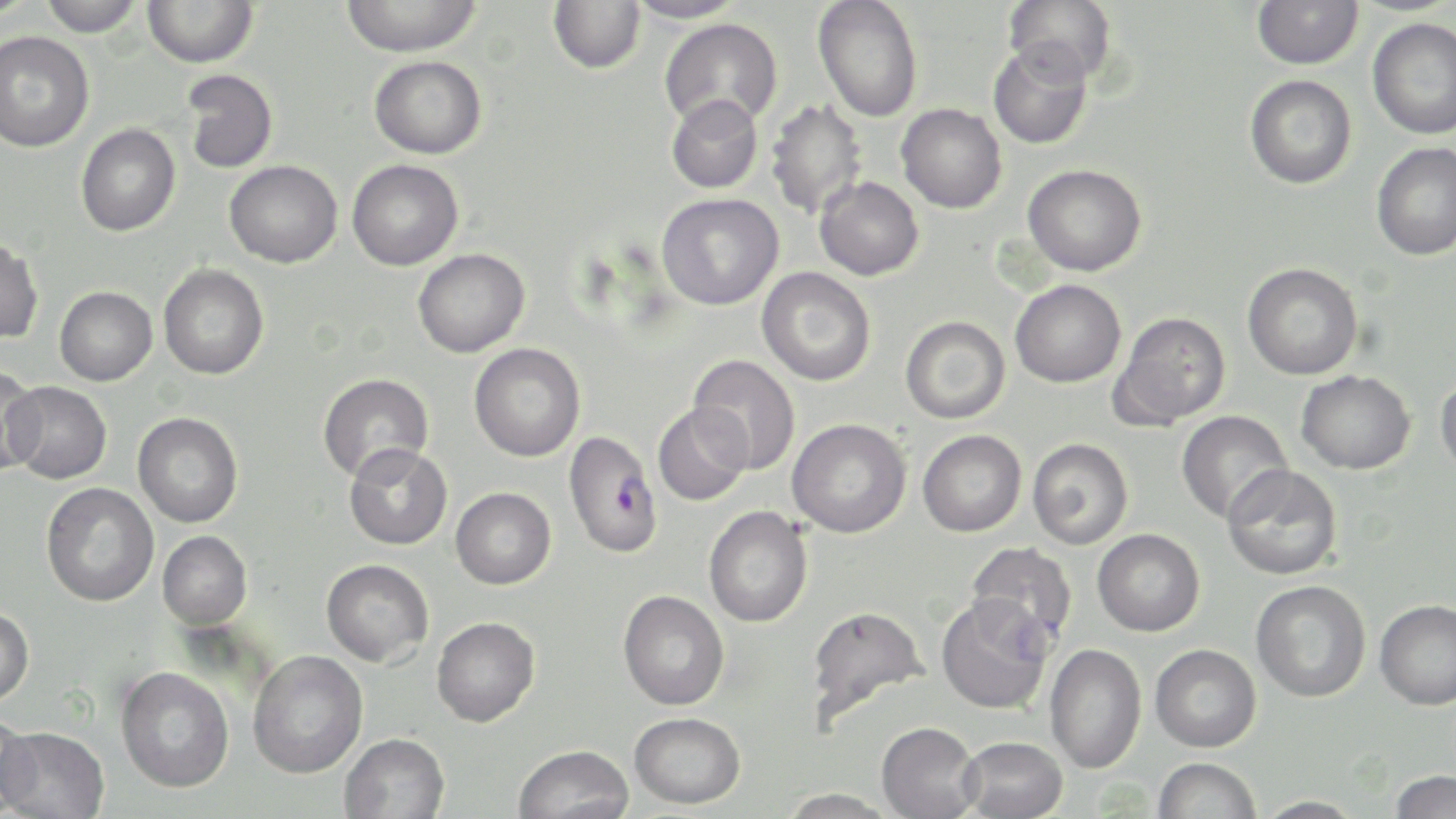
slide-level diagnosis = Plasmodium falciparum
stain = May-Grünwald-Giemsa
modality = optical microscopy
image size = 1456×819 pixels
uninfected red blood cell locations = approximate bounding boxes as [x1, y1, x2, y2] in pixels: [0, 0, 38, 21], [38, 0, 144, 37], [143, 0, 258, 68], [340, 0, 483, 56], [548, 0, 645, 74], [625, 0, 745, 24], [813, 0, 923, 123], [1004, 0, 1117, 84], [1252, 0, 1364, 70], [659, 18, 783, 129], [1367, 18, 1456, 139], [0, 31, 94, 153], [988, 40, 1093, 149], [369, 55, 487, 159], [182, 70, 278, 174], [1244, 75, 1357, 189], [666, 95, 763, 193], [765, 99, 867, 219], [896, 103, 1007, 214], [76, 123, 180, 237], [1371, 141, 1456, 260], [347, 159, 464, 271], [224, 160, 342, 268], [1022, 164, 1147, 276], [815, 177, 924, 281], [657, 193, 784, 311], [0, 238, 44, 343], [413, 248, 530, 358], [1242, 263, 1363, 380], [158, 264, 270, 380], [757, 267, 876, 386], [1010, 279, 1126, 387], [54, 286, 157, 386], [1109, 312, 1231, 430], [900, 316, 1010, 424], [469, 343, 585, 462], [688, 354, 801, 474], [0, 366, 43, 475], [1296, 370, 1416, 475], [317, 373, 434, 484], [1436, 373, 1456, 480], [5, 380, 113, 484], [653, 403, 752, 506], [1175, 410, 1293, 523], [132, 412, 243, 528], [787, 418, 911, 538], [918, 429, 1027, 537], [1027, 437, 1134, 550], [344, 443, 453, 550], [1222, 463, 1343, 580], [41, 482, 159, 607], [451, 487, 556, 589], [703, 506, 813, 627], [1092, 528, 1205, 636], [158, 531, 253, 629], [965, 542, 1078, 650], [321, 558, 433, 667], [1250, 580, 1371, 702], [618, 590, 729, 710], [935, 593, 1054, 714], [1375, 599, 1456, 710], [805, 604, 929, 728], [0, 606, 34, 706], [431, 616, 540, 727], [1045, 643, 1147, 773], [1150, 643, 1261, 752], [248, 650, 368, 778], [115, 666, 234, 793], [0, 709, 36, 818], [629, 712, 746, 809], [876, 721, 982, 819], [0, 726, 110, 818], [340, 732, 450, 819], [959, 736, 1068, 819], [513, 744, 635, 819], [1153, 757, 1262, 819], [1389, 769, 1456, 818], [778, 787, 897, 818], [1251, 796, 1368, 818]
preparation = thin blood smear
magnification = 1000x
field of view = one of a larger specimen
Plasmodium falciparum-infected red blood cell locations = approximate bounding boxes as [x1, y1, x2, y2] in pixels: [563, 431, 663, 558]